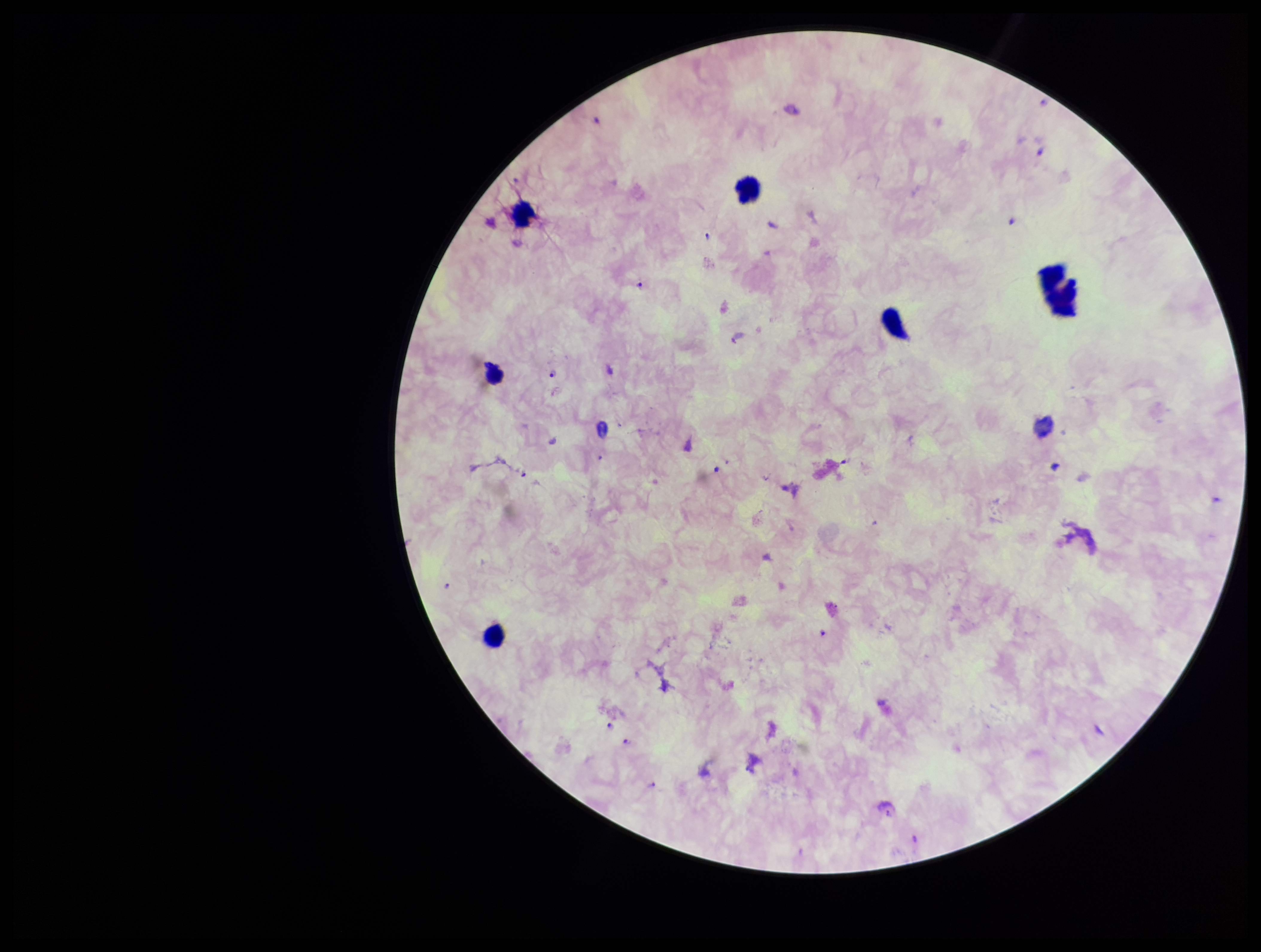 Plasmodium parasites: identified. Leukocyte count: 6. One field from this slide. Patient malaria status: positive. Image is 1261×952 pixels. Parasite count: 11. Smartphone photograph taken through the eyepiece of a microscope. Preparation: thick smear. Species reported for this patient: Plasmodium falciparum. Stained with Giemsa.